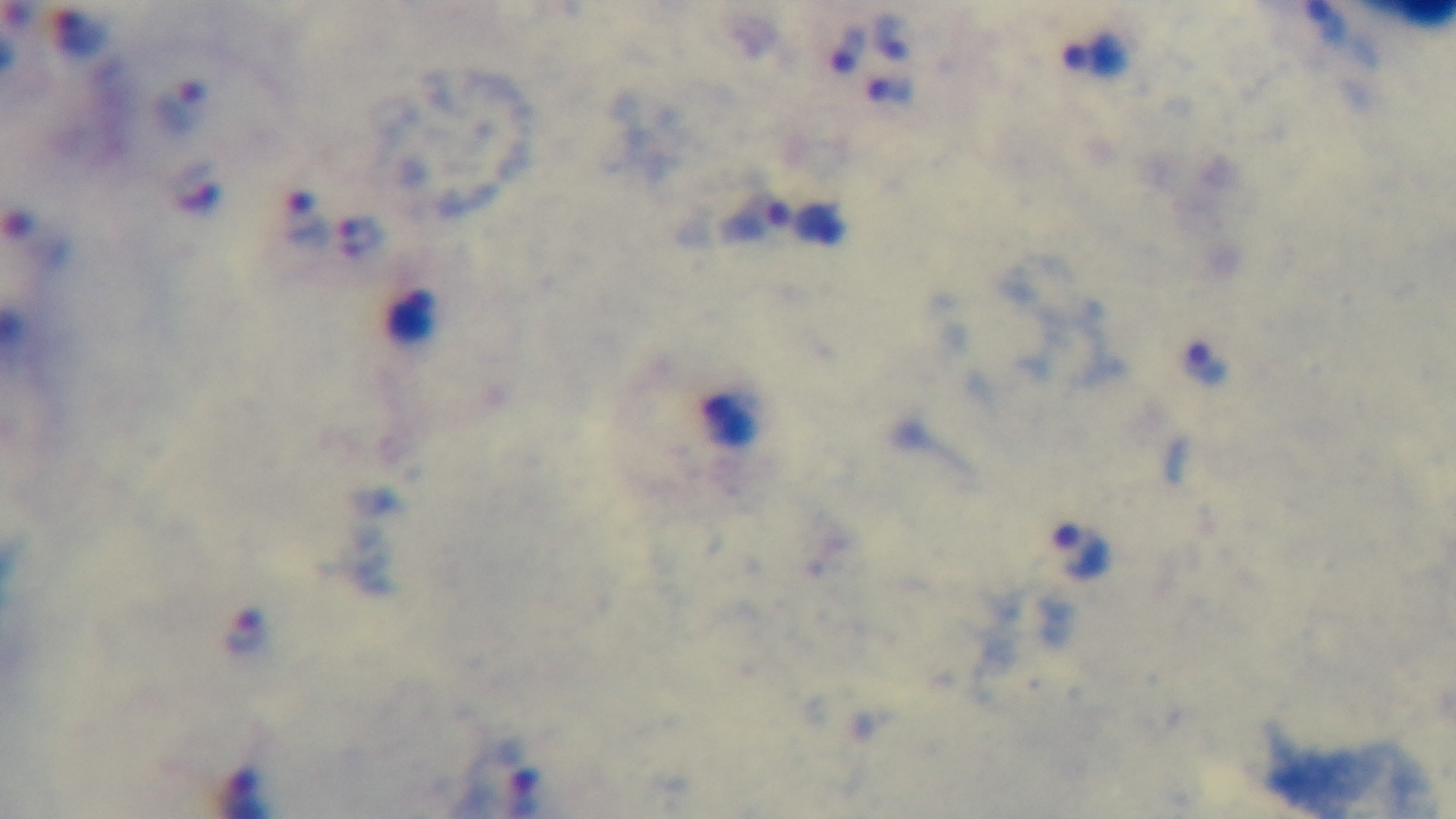

Summary:
  - Preparation: thick
  - Capture: mounted 4K digital camera
  - Objective: 100x oil immersion
  - Stain: Giemsa
  - Malaria status: positive
  - Modality: light microscopy
  - Field of view: single